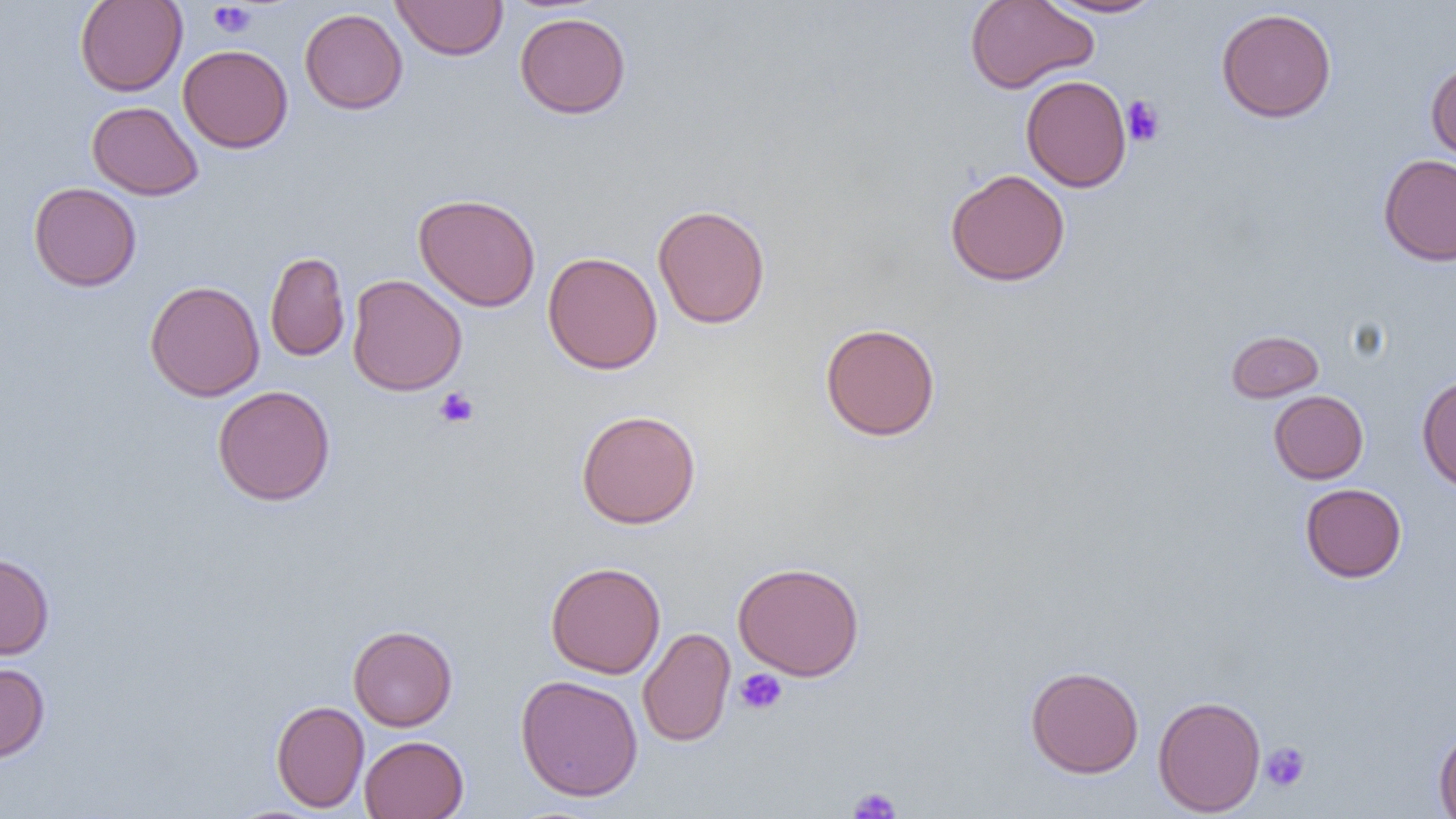

{
  "slide_level_diagnosis": "no evidence of blood parasites",
  "field_of_view": "single",
  "image_size": "1456×819 pixels",
  "magnification": "1000x",
  "uninfected_red_blood_cell_locations": "approximate bounding boxes as [x1, y1, x2, y2] in pixels: [74, 0, 187, 96], [392, 0, 508, 60], [965, 0, 1098, 93], [1040, 1, 1167, 18], [299, 8, 408, 114], [1216, 8, 1337, 123], [515, 12, 631, 119], [178, 44, 293, 153], [1426, 61, 1456, 164], [1021, 74, 1132, 192], [87, 100, 203, 201], [1378, 154, 1456, 266], [945, 168, 1070, 287], [28, 182, 142, 291], [413, 193, 541, 311], [652, 204, 770, 329], [265, 251, 350, 362], [543, 251, 663, 375], [347, 274, 467, 396], [144, 280, 265, 401], [820, 322, 941, 441], [1226, 330, 1324, 402], [1416, 374, 1456, 492], [212, 385, 336, 506], [1268, 390, 1369, 484], [575, 409, 701, 529], [1300, 483, 1407, 582], [0, 553, 54, 660], [545, 561, 666, 678], [732, 561, 865, 681], [348, 624, 458, 731], [638, 627, 735, 747], [0, 662, 50, 763], [1025, 665, 1144, 778], [515, 674, 644, 801], [1152, 695, 1266, 816], [271, 700, 369, 812], [1434, 729, 1456, 817], [359, 735, 468, 819]",
  "preparation": "thin blood film",
  "modality": "light microscopy",
  "platelet_locations": "approximate bounding boxes as [x1, y1, x2, y2] in pixels: [209, 2, 256, 38], [1122, 95, 1166, 147], [434, 387, 479, 428], [735, 668, 787, 715], [1260, 741, 1310, 793], [847, 786, 902, 818]"
}